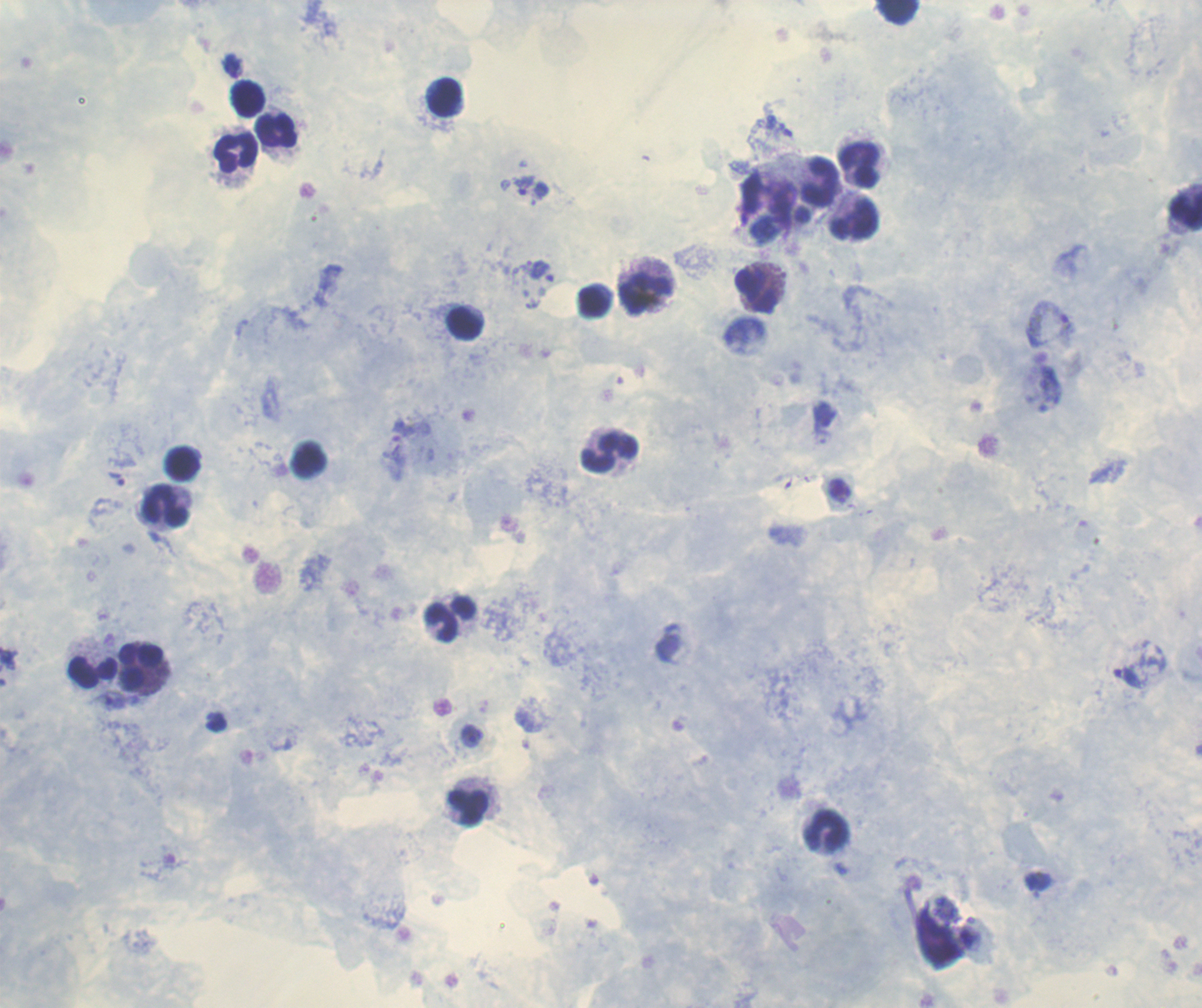
Approximate centers as [x, y] in pixels.
Summary:
  - Trophozoite locations: [523, 185], [537, 267], [1050, 322], [116, 478], [471, 735]
  - Leukocyte locations: [897, 12], [445, 96], [247, 97], [278, 132], [236, 153], [861, 164], [819, 179], [1187, 207], [856, 221], [756, 290], [594, 300], [465, 321], [608, 449], [308, 458], [181, 461], [165, 504], [449, 617], [92, 668], [143, 668], [467, 807], [826, 831]
  - Result: positive for malaria parasites
  - Image size: 1202×1008 pixels
  - Coloration quality: good
  - Field of view: one from this slide
  - Preparation: thick blood film
  - Background quality: good
  - Magnification: 100x
  - Stain: Romanowsky
  - Context: previously used in an actual diagnosis